Report the malaria status of this cell.
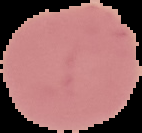

Uninfected.

Image is 142×133 pixels. Cell region segmented out of the field of view; the surrounding area is masked to black. From a thin blood smear.